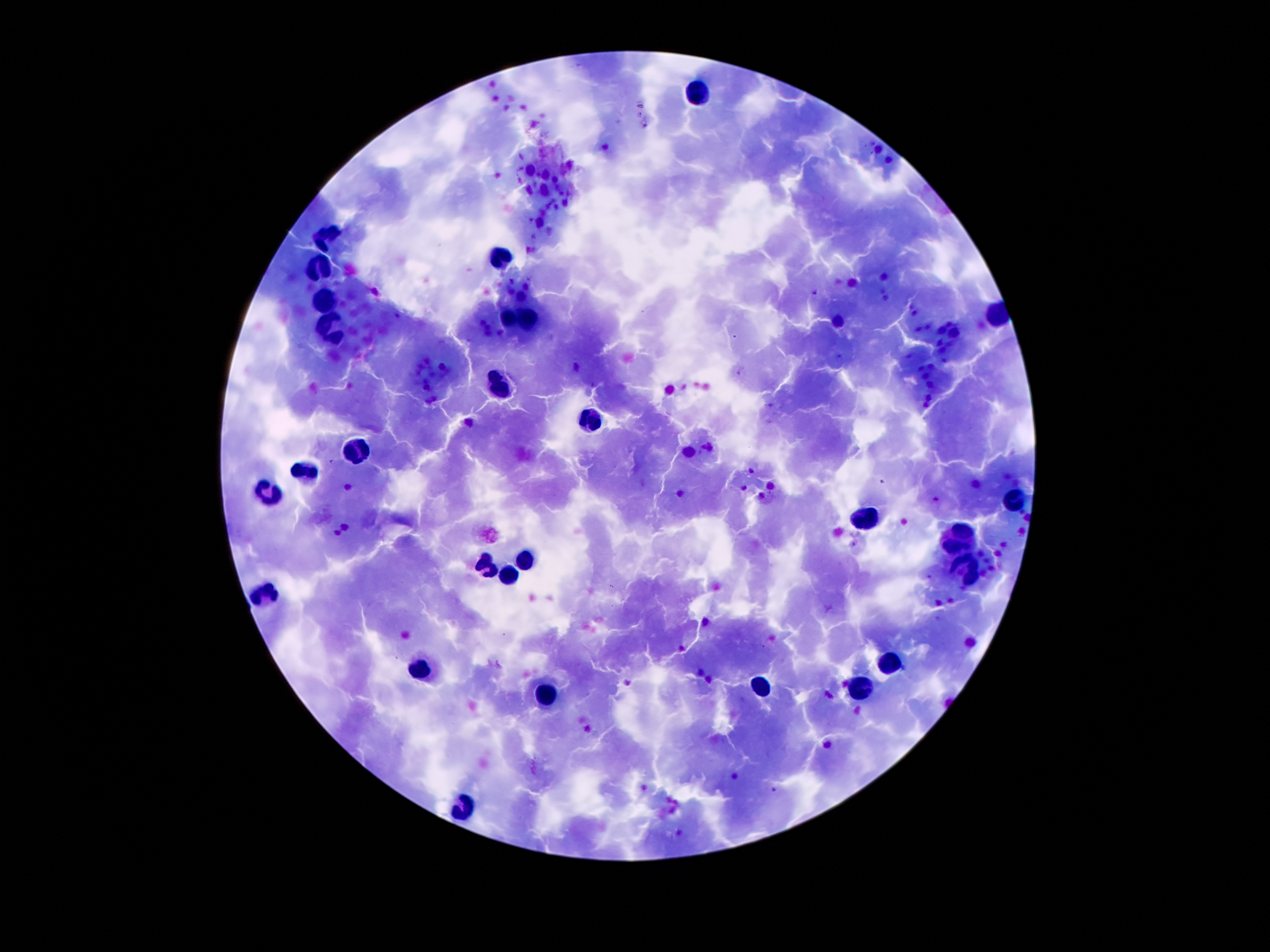
coordinate format = approximate centers as (x, y) in pixels
Plasmodium parasite locations = (937, 499)
leukocyte locations = (696, 90), (330, 231), (506, 255), (316, 266), (327, 298), (506, 317), (531, 317), (330, 326), (502, 381), (586, 423), (356, 455), (312, 469), (272, 494), (1018, 499), (871, 514), (959, 532), (487, 560), (524, 564), (966, 565), (506, 571), (264, 594), (414, 666), (893, 666), (860, 688), (762, 689), (550, 695), (462, 806)
stain = Giemsa
patient malaria status = infected with Plasmodium falciparum
field of view = one from this slide
preparation = thick blood film
image size = 1270×952 pixels
capture = smartphone camera through the microscope eyepiece
magnification = 100x